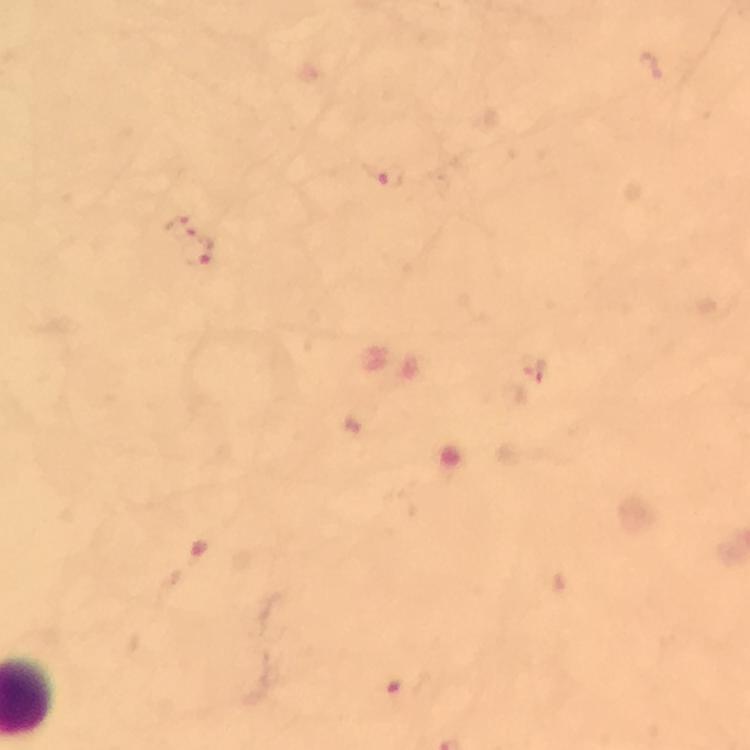
immersion oil = used
magnification = 100x
preparation = thick blood film
context = from a malaria diagnostic workup
cropped from = one field of view
image size = 750×750 pixels
stain = Giemsa
capture = smartphone camera through the microscope
Plasmodium parasite locations = approximate object centers, in pixels from the top-left corner: (x=387, y=177), (x=180, y=226), (x=199, y=253), (x=533, y=367), (x=393, y=686)